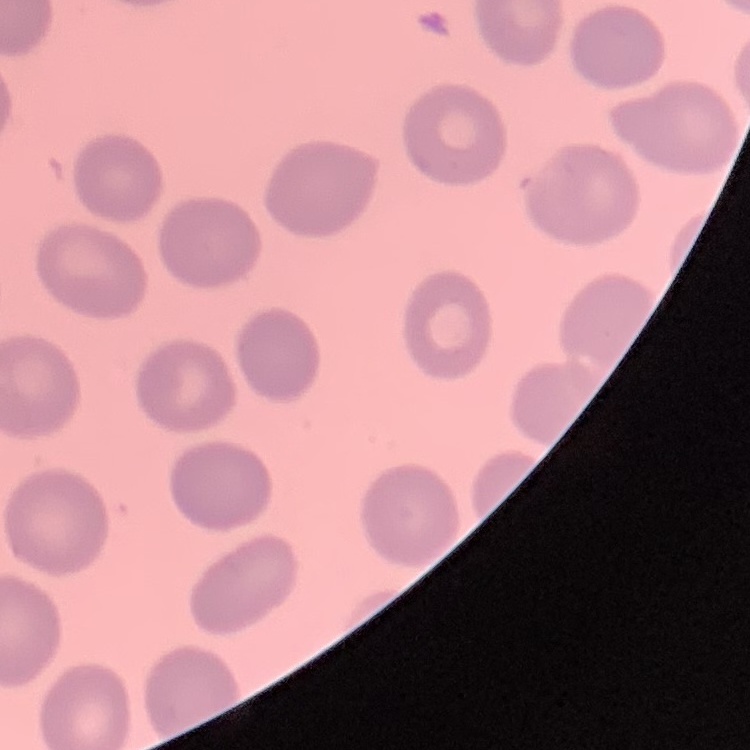
Summary:
  - Erythrocyte morphology: no rouleaux formation
  - Image type: square crop of a larger photomicrograph
  - Stain: Field's or Giemsa
  - Preparation: thin blood smear